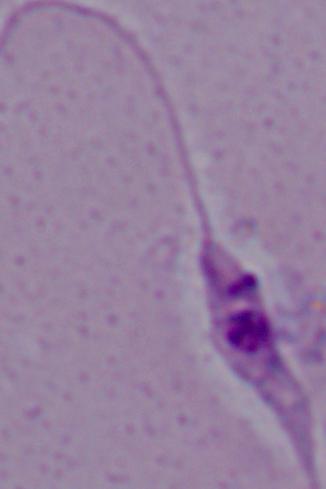

magnification = 1000x
identification = Leishmania
modality = micrograph